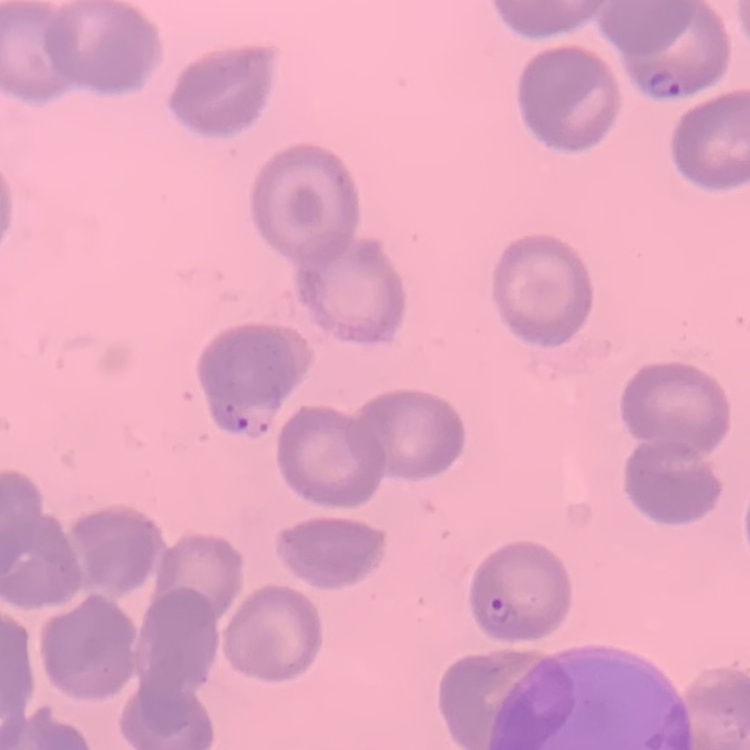

The erythrocytes exhibit no rouleaux formation. Stained with either Field's or Giemsa. Thin blood film. Square crop of a larger photomicrograph.